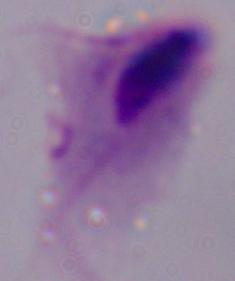
Summary:
  - Magnification: 1000x
  - Identification: trichomonad
  - Modality: micrograph